Classify the preparation.
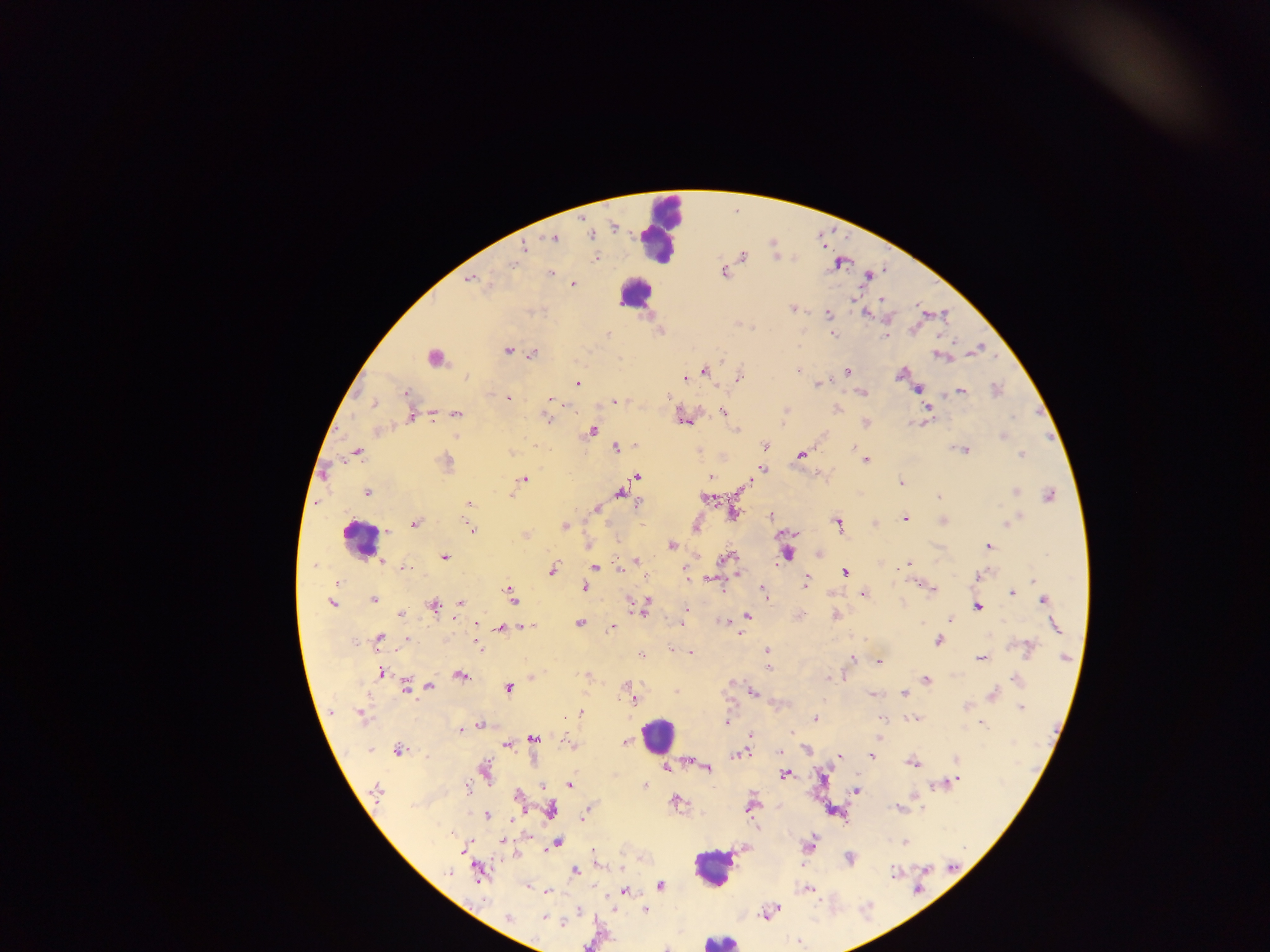

Thick blood film.

{
  "capture": "mobile-phone photograph through a microscope",
  "leukocyte_locations": "approximate centers as {x, y} in pixels: {662, 227}, {635, 295}, {436, 357}, {358, 536}, {656, 737}, {712, 866}, {720, 941}",
  "field_of_view": "single",
  "image_size": "1270×952 pixels",
  "malaria_parasite_locations": "approximate centers as {x, y} in pixels: {614, 228}, {592, 235}, {553, 239}, {525, 247}, {743, 256}, {596, 259}, {514, 264}, {724, 271}, {551, 272}, {868, 276}, {470, 278}, {572, 283}, {852, 299}, {881, 300}, {792, 309}, {828, 315}, {866, 315}, {604, 334}, {833, 334}, {885, 335}, {508, 350}, {533, 354}, {942, 357}, {620, 358}, {798, 370}, {703, 371}, {847, 371}, {900, 374}, {466, 376}, {739, 376}, {684, 378}, {578, 383}, {817, 384}, {917, 389}, {997, 389}, {961, 391}, {405, 392}, {861, 393}, {508, 398}, {551, 399}, {668, 399}, {554, 402}, {615, 402}, {373, 403}, {927, 408}, {838, 410}, {725, 412}, {456, 414}, {1013, 417}, {412, 418}, {548, 419}, {684, 420}, {865, 423}, {735, 430}, {591, 431}, {1002, 436}, {765, 445}, {853, 447}, {615, 448}, {964, 451}, {356, 452}, {511, 453}, {801, 455}, {1022, 455}, {865, 460}, {446, 462}, {762, 469}, {636, 477}, {710, 477}, {524, 480}, {900, 483}, {744, 487}, {1015, 491}, {367, 492}, {621, 492}, {1049, 495}, {939, 496}, {707, 498}, {640, 503}, {469, 504}, {597, 508}, {734, 513}, {771, 516}, {1016, 518}, {906, 519}, {942, 521}, {1007, 523}, {414, 524}, {838, 525}, {564, 526}, {696, 527}, {472, 529}, {387, 531}, {525, 534}, {671, 545}, {988, 546}, {787, 554}, {445, 557}, {727, 558}, {382, 560}, {616, 560}, {637, 562}, {909, 564}, {314, 565}, {595, 567}, {406, 568}, {553, 569}, {846, 572}, {981, 574}, {711, 580}, {1034, 580}, {806, 581}, {338, 582}, {584, 587}, {932, 589}, {763, 591}, {1011, 593}, {862, 594}, {511, 595}, {1044, 599}, {373, 600}, {649, 600}, {460, 602}, {332, 604}, {645, 605}, {434, 607}, {978, 607}, {686, 609}, {401, 615}, {747, 615}, {799, 616}, {835, 616}, {950, 619}, {723, 621}, {579, 623}, {680, 623}, {476, 624}, {1055, 625}, {526, 627}, {501, 628}, {612, 628}, {379, 638}, {406, 639}, {938, 641}, {477, 645}, {1027, 648}, {671, 649}, {767, 650}, {691, 653}, {640, 655}, {1066, 657}, {981, 658}, {853, 659}, {878, 661}, {769, 667}, {382, 672}, {460, 675}, {830, 678}, {1016, 680}, {926, 681}, {735, 683}, {627, 686}, {406, 687}, {412, 687}, {431, 687}, {509, 688}, {676, 692}, {752, 692}, {904, 694}, {871, 695}, {993, 695}, {633, 699}, {965, 706}, {1021, 707}, {362, 714}, {580, 714}, {815, 718}, {883, 719}, {913, 719}, {726, 722}, {481, 724}, {982, 725}, {460, 731}, {790, 732}, {751, 734}, {534, 738}, {569, 743}, {623, 743}, {507, 744}, {398, 750}, {371, 751}, {740, 753}, {840, 756}, {871, 756}, {956, 760}, {912, 762}, {706, 766}, {666, 768}, {485, 770}, {785, 774}, {957, 780}, {569, 785}, {938, 785}, {542, 786}, {645, 786}, {468, 789}, {376, 790}, {856, 791}, {517, 795}, {675, 800}, {751, 806}, {898, 809}, {552, 811}, {486, 815}, {583, 815}, {503, 841}, {557, 843}, {904, 843}, {809, 844}, {465, 847}, {849, 858}, {576, 870}, {926, 870}, {448, 872}, {479, 872}, {893, 873}, {660, 886}, {527, 887}, {808, 888}, {624, 891}, {547, 892}, {645, 909}, {769, 912}, {508, 918}, {543, 918}, {562, 923}, {798, 942}",
  "country": "Ghana"
}